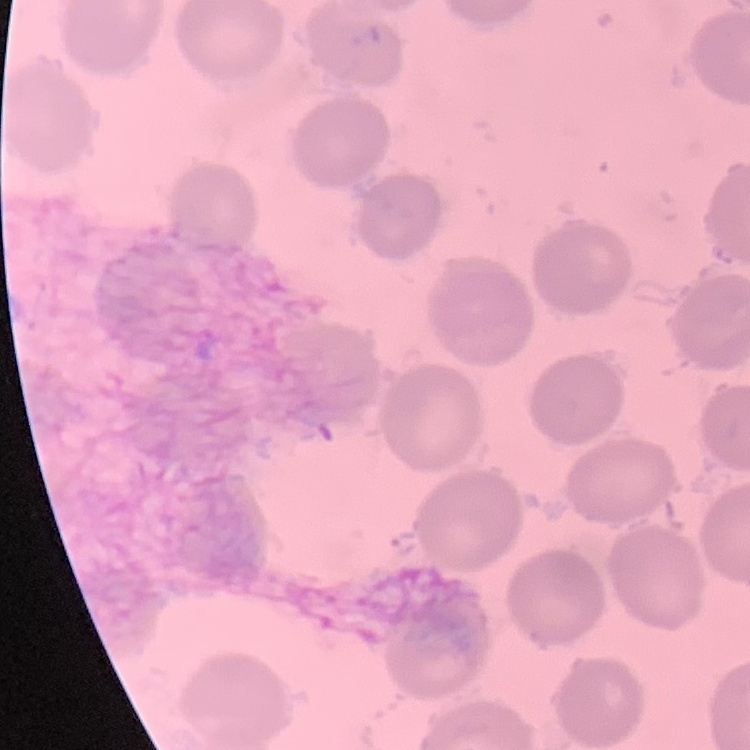
erythrocyte morphology = no rouleaux formation
stain = Field's or Giemsa
image type = one tile cut from a larger photomicrograph
preparation = thin blood smear